Report the malaria status of this cell.
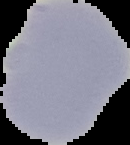
It is uninfected.

preparation: thin blood smear
image_type: segmented cell region with the area outside set to black
image_size: 130×145 pixels